Classify this cell by malaria status.
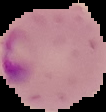
Parasitized.

Segmented cell region on a black background. From a thin blood film. Image is 106×112 pixels.